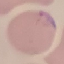

Malaria status: parasitized. Cell patch, automatically extracted from a larger field of view and resized to 64 × 64 pixels. Acquired by smartphone through the microscope eyepiece. Thin smear of blood. Giemsa-stained preparation.